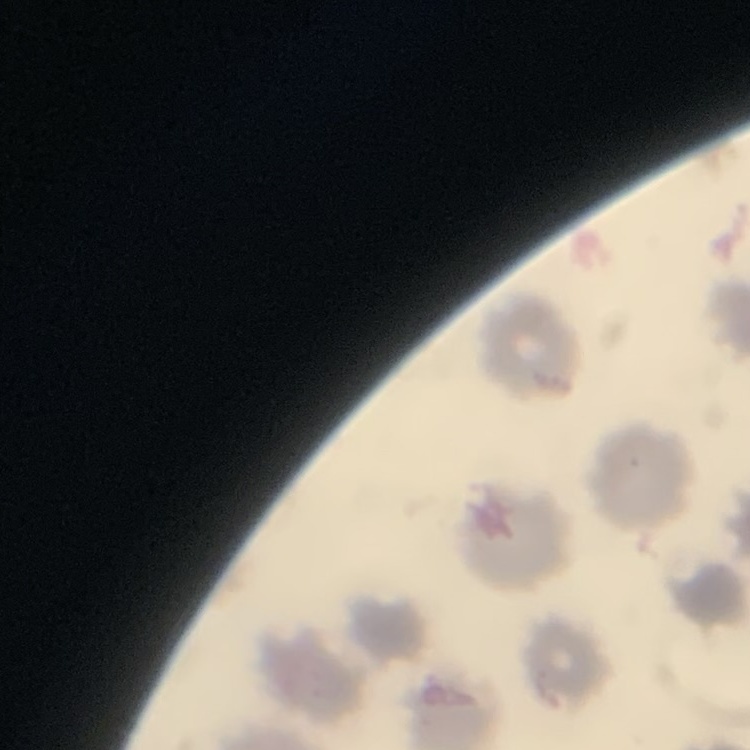

erythrocyte morphology = no rouleaux formation
preparation = thin blood film
stain = Field's or Giemsa
image type = one tile cut from a larger photomicrograph